Report the malaria status of this cell.
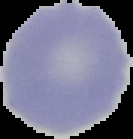
It is uninfected.

The area outside the segmented cell region is set to black. Image is 133×139 pixels. From a thin blood smear.